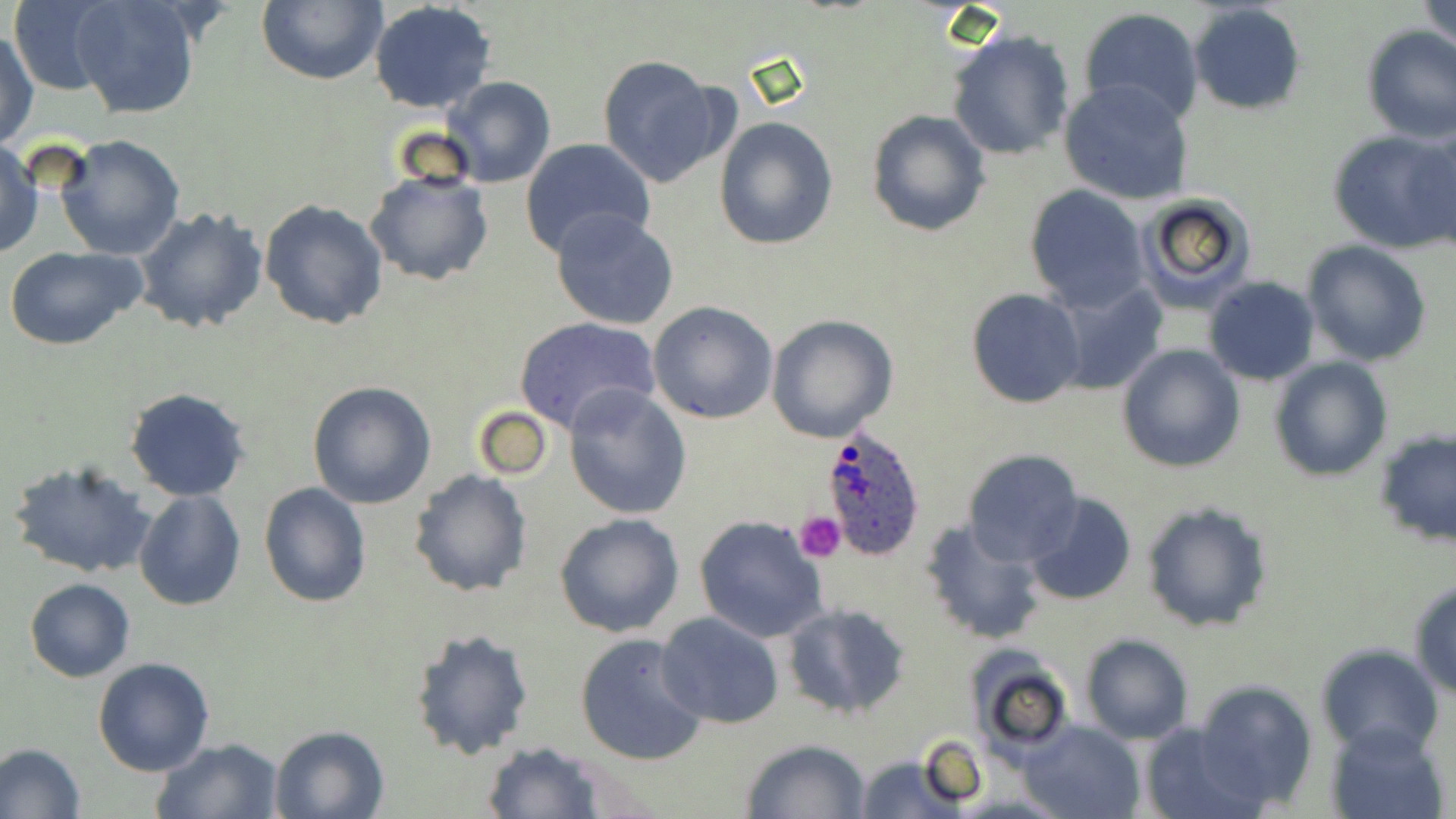
Approximate bounding boxes as [x1, y1, x2, y2] in pixels. Platelet locations: [796, 510, 846, 562]. Plasmodium ovale-infected red blood cell locations: [819, 422, 928, 559]. Uninfected red blood cell locations: [255, 0, 386, 86], [369, 0, 496, 114], [1422, 0, 1455, 57], [8, 1, 113, 95], [70, 1, 200, 120], [1187, 3, 1308, 115], [1078, 9, 1206, 126], [948, 27, 1074, 161], [1361, 27, 1456, 144], [1, 29, 38, 151], [596, 55, 729, 187], [442, 76, 555, 187], [1059, 79, 1195, 206], [866, 110, 991, 238], [714, 117, 839, 250], [1328, 127, 1456, 254], [1405, 127, 1456, 254], [56, 134, 185, 260], [519, 137, 656, 258], [1, 140, 43, 259], [364, 169, 494, 287], [1023, 185, 1149, 313], [1133, 194, 1257, 312], [259, 199, 389, 331], [134, 207, 269, 335], [550, 208, 680, 331], [1301, 239, 1433, 365], [3, 245, 148, 350], [1202, 275, 1321, 386], [1055, 280, 1167, 395], [967, 287, 1086, 408], [648, 300, 779, 424], [765, 315, 897, 442], [512, 316, 662, 433], [1117, 343, 1245, 473], [1270, 356, 1394, 480], [307, 380, 438, 509], [563, 384, 691, 519], [124, 388, 252, 501], [473, 406, 552, 482], [1375, 433, 1455, 547], [962, 449, 1085, 567], [6, 457, 158, 580], [408, 469, 533, 598], [258, 481, 372, 607], [133, 490, 247, 610], [1024, 492, 1136, 607], [1141, 500, 1275, 633], [554, 513, 684, 638], [694, 514, 830, 644], [920, 518, 1049, 645], [24, 578, 136, 682], [1408, 578, 1456, 699], [781, 602, 914, 718], [655, 611, 784, 730], [409, 627, 534, 759], [574, 633, 710, 766], [1080, 634, 1194, 744], [1314, 643, 1443, 755], [964, 652, 1075, 757], [92, 657, 215, 775], [1191, 678, 1317, 809], [1018, 720, 1145, 819], [1138, 721, 1263, 818], [1329, 721, 1451, 819], [269, 724, 389, 819], [150, 737, 286, 819], [740, 738, 872, 819], [481, 742, 609, 818], [0, 744, 85, 817], [856, 754, 961, 818]. Slide-level diagnosis: Plasmodium ovale. Light microscopy. Image is 1456×819 pixels. Single field of view. May-Grünwald-Giemsa stain. 1000x magnification. Thin blood film.